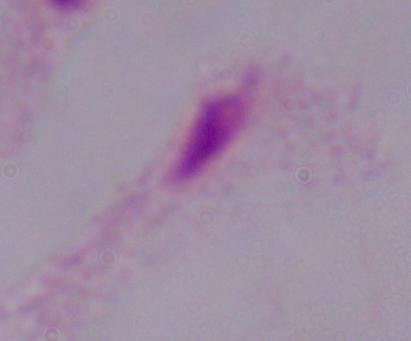

magnification: 1000x
modality: photomicrograph
identification: trichomonad